Identify the parasite.
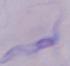
A trypanosome.

Summary:
  - Modality: micrograph
  - Magnification: 1000x